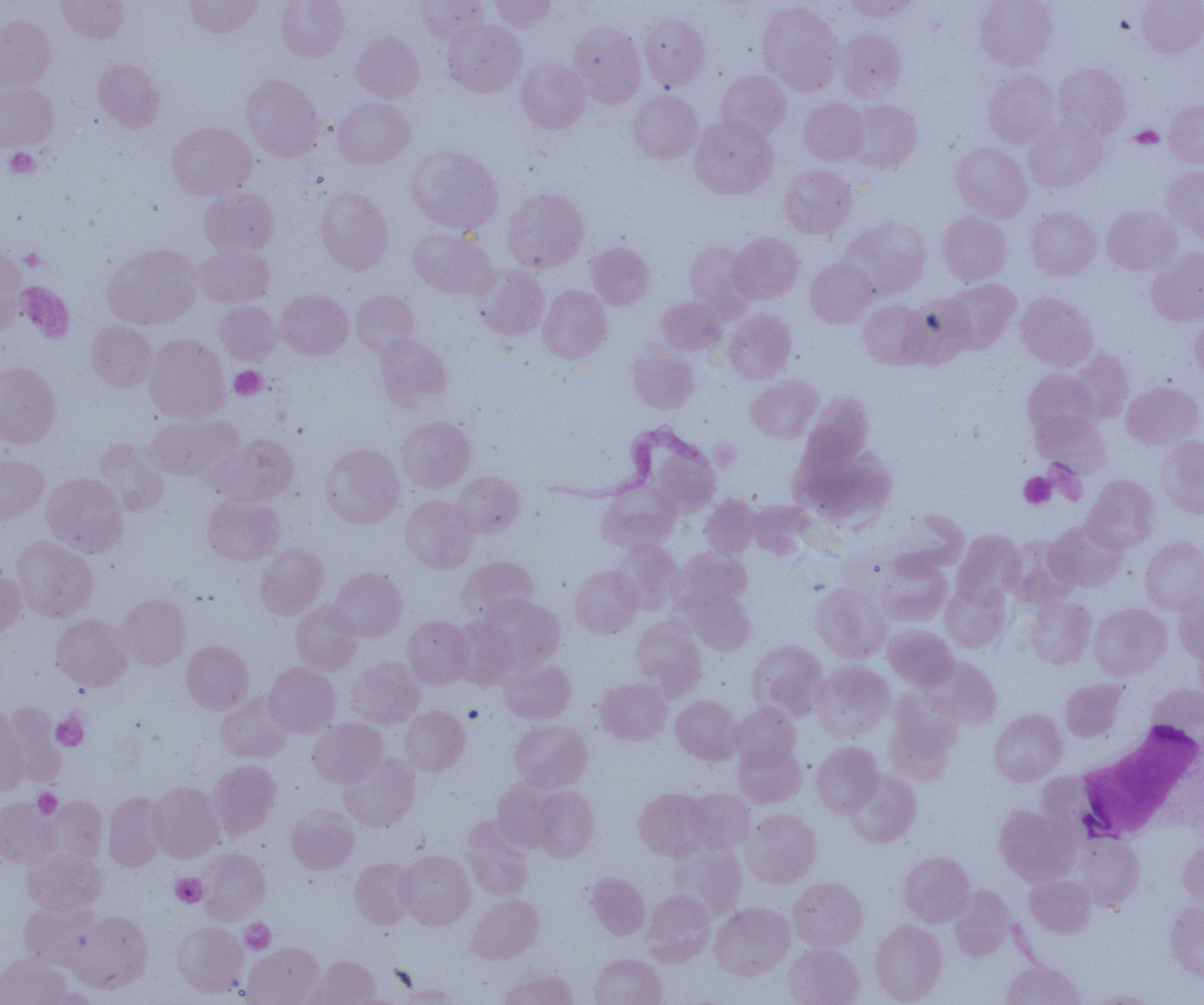
Approximate bounding boxes as (x1,y1)-(x2,y2) corner pairs in pixels. Platelet locations: (1129,126)-(1163,148), (5,148)-(39,178), (20,248)-(45,270), (19,282)-(78,342), (230,366)-(267,399), (1019,472)-(1056,509), (52,712)-(88,750), (33,789)-(62,819), (171,873)-(207,907), (240,919)-(275,953). White blood cell locations: (1076,721)-(1203,841). Uninfected red blood cell locations: (56,0)-(129,43), (184,0)-(263,38), (276,0)-(349,61), (416,0)-(489,44), (489,0)-(555,32), (843,0)-(916,22), (975,0)-(1057,70), (1137,0)-(1204,58), (757,1)-(842,93), (639,13)-(710,90), (0,15)-(55,90), (442,20)-(526,96), (569,23)-(645,106), (835,28)-(907,101), (352,32)-(424,102), (516,57)-(590,133), (92,59)-(165,133), (1053,63)-(1131,140), (983,69)-(1059,148), (715,70)-(791,141), (241,75)-(324,161), (0,83)-(58,151), (628,90)-(702,164), (332,97)-(415,169), (799,97)-(868,165), (847,99)-(922,171), (1164,99)-(1204,168), (690,115)-(778,199), (1024,115)-(1108,192), (167,121)-(256,199), (951,142)-(1032,222), (405,145)-(503,233), (779,165)-(857,238), (1163,166)-(1204,242), (314,186)-(393,274), (199,188)-(278,257), (503,188)-(588,272), (1102,205)-(1182,275), (1026,208)-(1101,280), (937,211)-(1011,284), (839,218)-(931,299), (408,227)-(498,299), (728,232)-(803,304), (684,241)-(755,316), (586,242)-(654,310), (102,244)-(202,329), (193,245)-(274,307), (1146,247)-(1204,326), (0,250)-(27,332), (805,258)-(877,327), (473,264)-(549,340), (941,278)-(1020,354), (538,285)-(612,363), (276,289)-(353,359), (351,289)-(419,357), (1015,291)-(1098,371), (901,294)-(974,367), (657,298)-(726,355), (857,299)-(930,369), (215,300)-(280,364), (723,308)-(796,384), (1191,313)-(1204,383), (86,321)-(156,391), (375,334)-(452,411), (143,335)-(230,422), (628,345)-(699,414), (1069,348)-(1134,422), (0,361)-(60,449), (1023,369)-(1098,440), (746,376)-(822,443), (1122,380)-(1203,449), (800,394)-(873,472), (1033,411)-(1110,476), (142,415)-(236,481), (397,416)-(475,491), (215,434)-(299,505), (1156,436)-(1204,517), (95,438)-(169,516), (790,441)-(895,528), (321,443)-(404,528), (0,454)-(48,524), (42,472)-(128,557), (452,472)-(525,537), (1083,475)-(1159,552), (597,485)-(678,552), (202,494)-(285,566), (700,494)-(761,560), (400,495)-(478,572), (747,499)-(813,558), (1045,521)-(1127,592), (952,530)-(1026,603), (12,536)-(97,622), (1005,536)-(1079,609), (1140,537)-(1204,613), (611,540)-(682,612), (255,544)-(329,619), (673,548)-(751,611), (877,554)-(952,626), (457,556)-(538,622), (570,565)-(643,638), (330,567)-(407,641), (0,569)-(25,636), (940,579)-(1011,652), (810,582)-(891,662), (682,587)-(755,655), (1175,587)-(1204,662), (117,593)-(191,670), (475,594)-(565,673), (1024,597)-(1095,668), (291,601)-(363,673), (1089,603)-(1171,679), (51,614)-(132,691), (402,616)-(475,688), (631,617)-(706,697), (883,625)-(959,691), (1194,638)-(1204,705), (747,640)-(828,720), (181,641)-(253,714), (923,656)-(1002,728), (346,657)-(424,728), (499,660)-(576,724), (811,661)-(894,742), (265,662)-(340,737), (595,677)-(672,745), (1061,678)-(1127,741), (1147,683)-(1204,744), (217,692)-(294,762), (885,693)-(962,786), (671,695)-(743,764), (2,702)-(67,786), (731,702)-(801,769), (399,705)-(470,776), (0,707)-(29,795), (989,709)-(1067,785), (309,718)-(388,787), (509,719)-(593,791), (733,741)-(806,807), (812,741)-(883,816), (338,753)-(420,831), (208,759)-(281,839), (846,770)-(921,846), (492,777)-(565,850), (148,782)-(224,862), (528,785)-(599,861), (634,787)-(712,861), (683,788)-(755,853), (103,792)-(168,870), (45,795)-(107,865), (0,797)-(58,867), (286,805)-(359,873), (994,805)-(1077,885), (742,808)-(821,888), (461,815)-(535,899), (1074,834)-(1145,910), (1178,839)-(1204,907), (668,843)-(747,920), (23,847)-(105,914), (198,847)-(271,922), (397,849)-(475,929), (899,851)-(974,926), (350,858)-(420,928), (586,872)-(650,940), (1025,875)-(1095,937), (788,877)-(867,951), (949,886)-(1015,961), (642,890)-(715,965), (467,894)-(543,964), (1166,900)-(1204,980), (20,901)-(100,969), (710,902)-(795,979), (70,910)-(153,993), (870,919)-(947,1004), (172,921)-(248,998), (242,942)-(324,1005), (784,943)-(864,1005), (0,953)-(71,1005), (590,953)-(666,1005), (309,955)-(381,1004), (1003,959)-(1084,1005), (498,966)-(577,1005), (396,984)-(465,1004), (36,987)-(101,1004), (1088,990)-(1159,1005). Trypanosoma brucei locations: (535,420)-(719,508). Slide-level diagnosis: Trypanosoma brucei. Image is 1204×1005 pixels. One field of a larger specimen. 1000x magnification. Thin blood film. Optical microscopy.